Name the cell type shown.
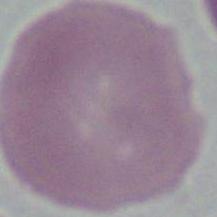

An erythrocyte.

magnification: 1000x
modality: photomicrograph